Classify this cell by malaria status.
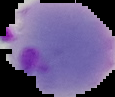

Parasitized.

image_type: segmented cell region on a black background
preparation: thin blood film
image_size: 115×97 pixels